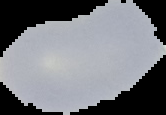
From a thin blood smear. Result: no malaria parasites seen. The area outside the segmented cell region is set to black. Image is 166×115 pixels.